Evaluate for malaria.
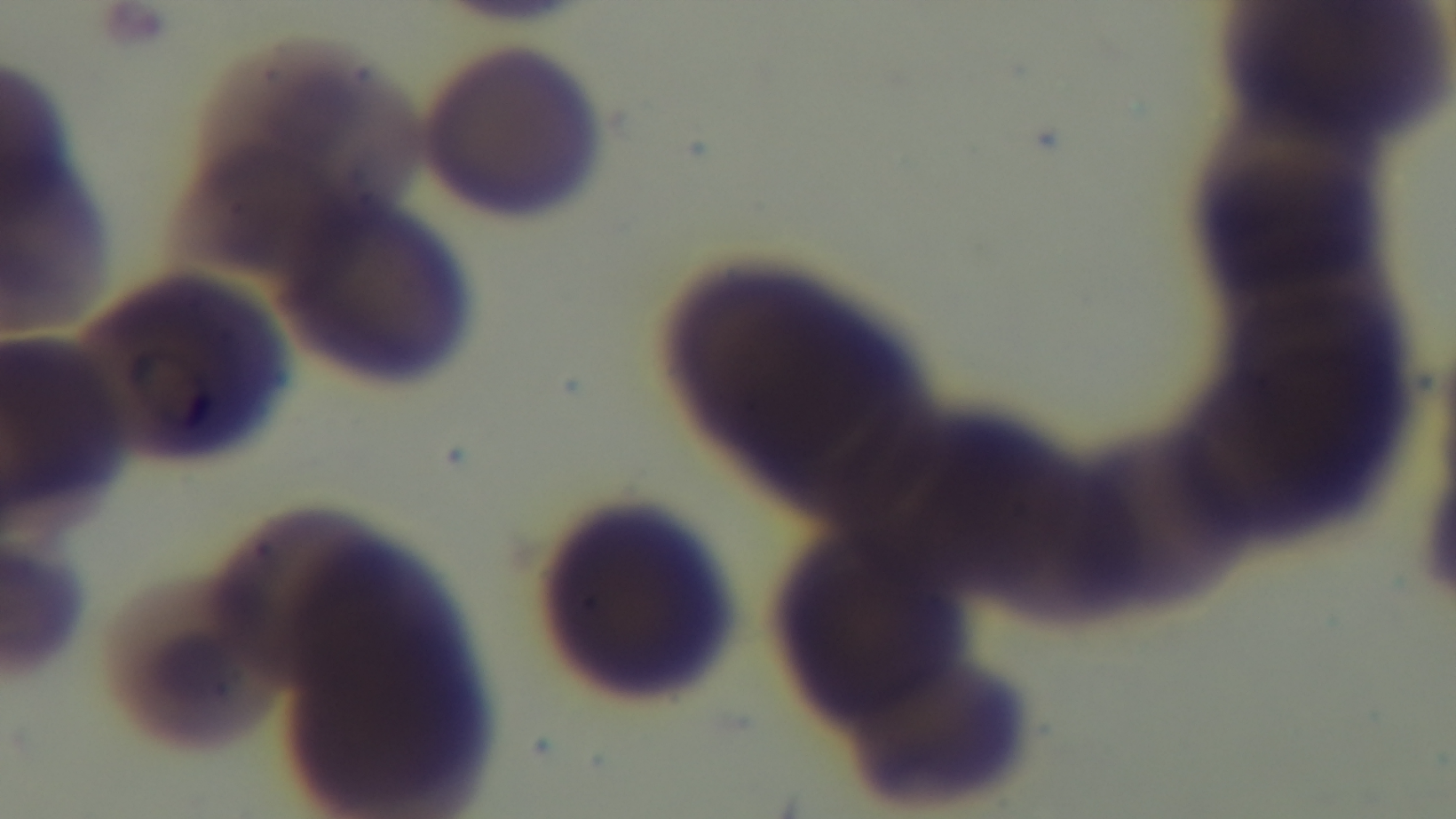

It is infected.

field of view = one from the slide
capture = mounted 4K digital camera
modality = light microscopy
objective = 100x oil immersion
stain = Giemsa
preparation = thin smear